Identify the cell.
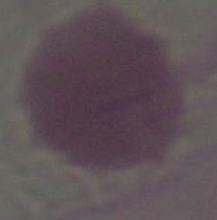
This is an erythrocyte.

Summary:
  - Modality: photomicrograph
  - Magnification: 1000x